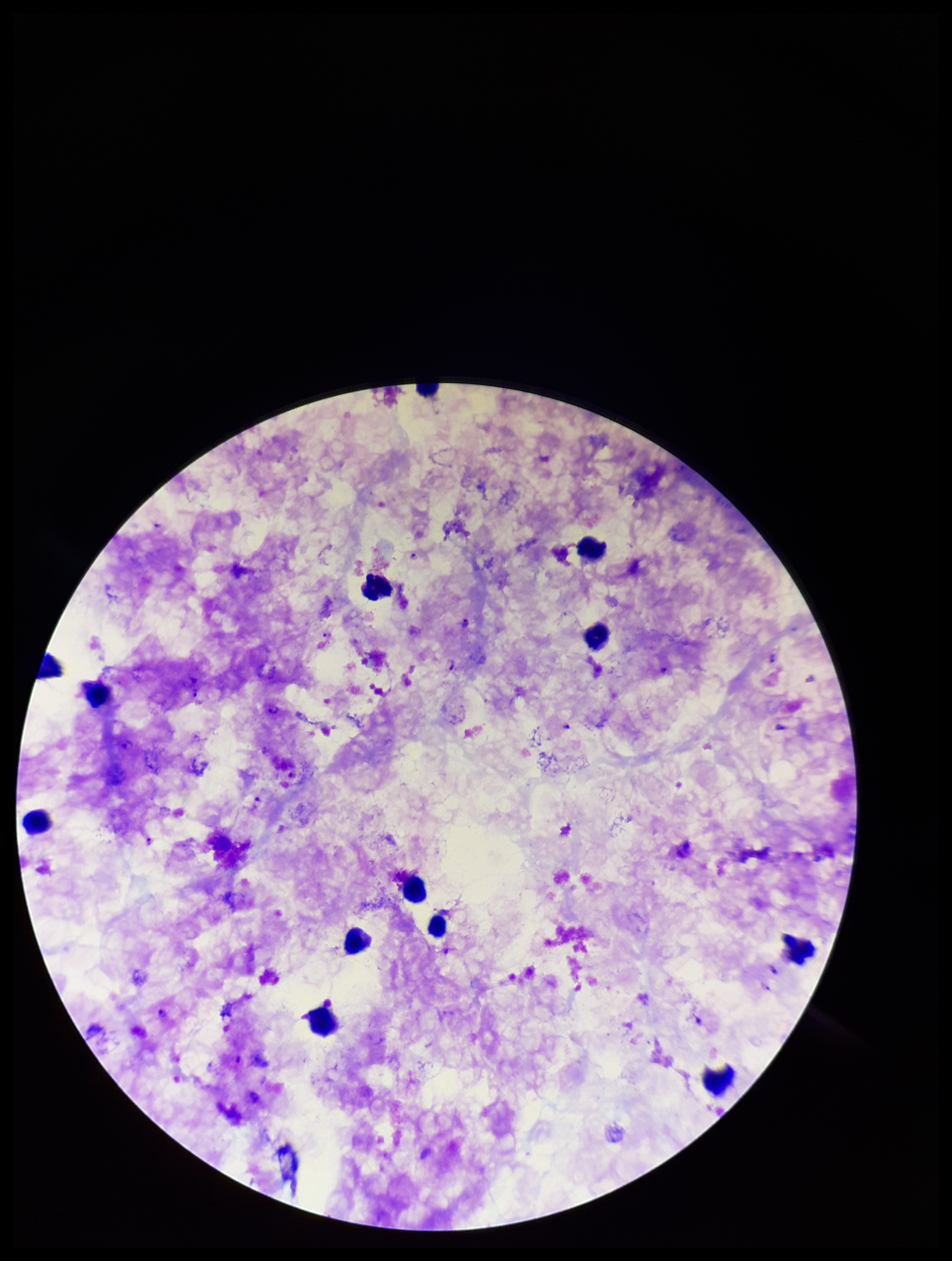

Giemsa stain. Parasite count: 6. Single field of view. Preparation: thick smear. Image is 952×1261 pixels. Smartphone photograph taken through the eyepiece of a microscope. Plasmodium parasites: identified. Leukocyte count: 12. Species reported for this patient: Plasmodium falciparum. Patient malaria status: infected.